Point out each leukocyte.
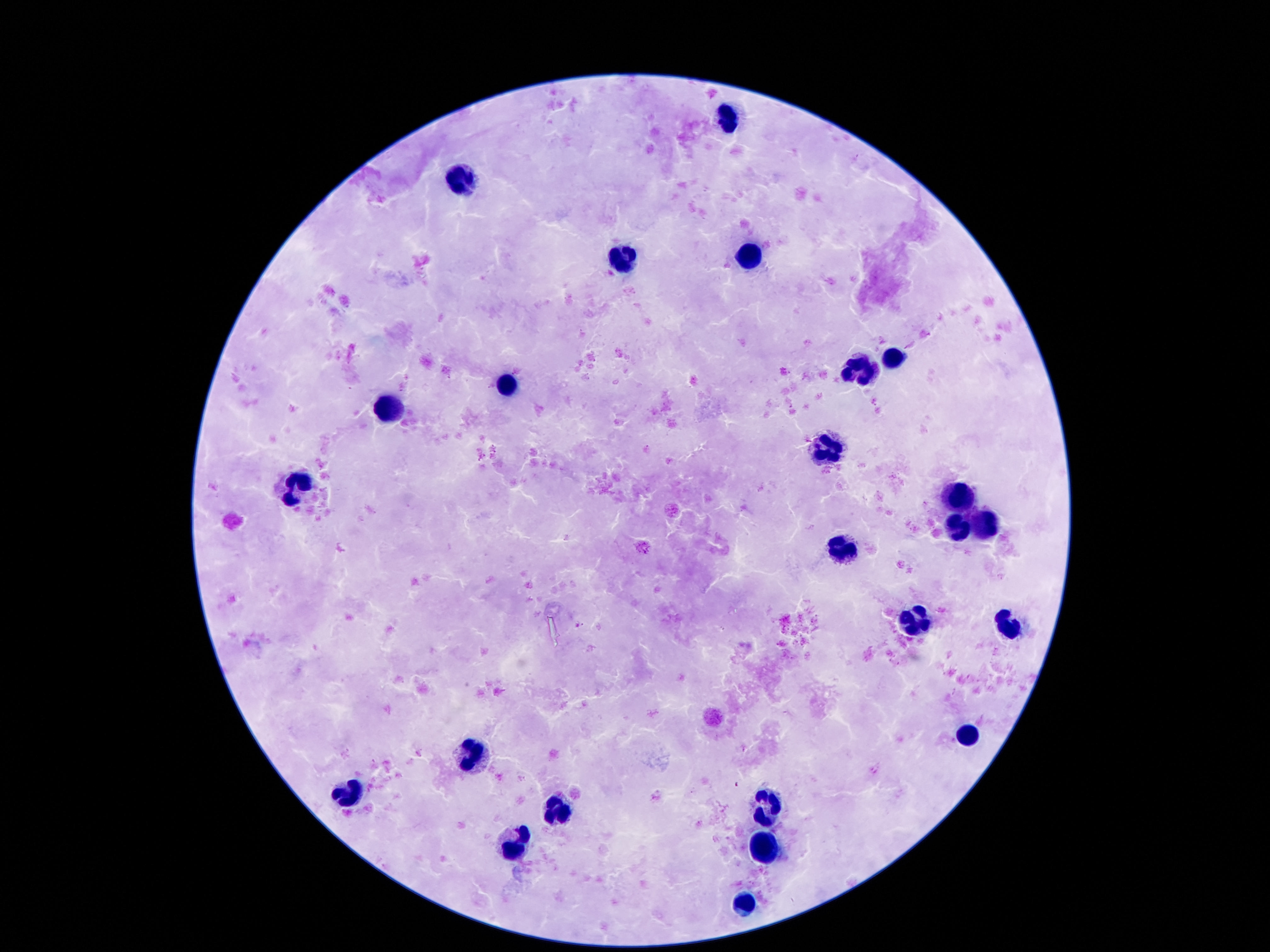

Approximate centers as {x, y} in pixels.
Leukocytes: {727, 113}, {461, 179}, {745, 254}, {620, 257}, {892, 356}, {860, 369}, {511, 385}, {391, 408}, {827, 447}, {293, 490}, {958, 497}, {986, 524}, {951, 529}, {849, 553}, {913, 620}, {1008, 628}, {965, 737}, {471, 755}, {352, 794}, {774, 805}, {554, 812}, {516, 839}, {765, 848}, {745, 907}.

capture = smartphone camera through the microscope eyepiece
patient malaria status = not infected
image size = 1270×952 pixels
magnification = 100x
preparation = thick blood smear
field of view = one from this slide
stain = Giemsa